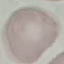

Summary:
  - Result: negative for malaria parasites
  - Preparation: thin blood smear
  - Capture: smartphone through the microscope eyepiece
  - Stain: Giemsa
  - Image type: cell patch, automatically extracted from a larger field of view and resized to 64 × 64 pixels